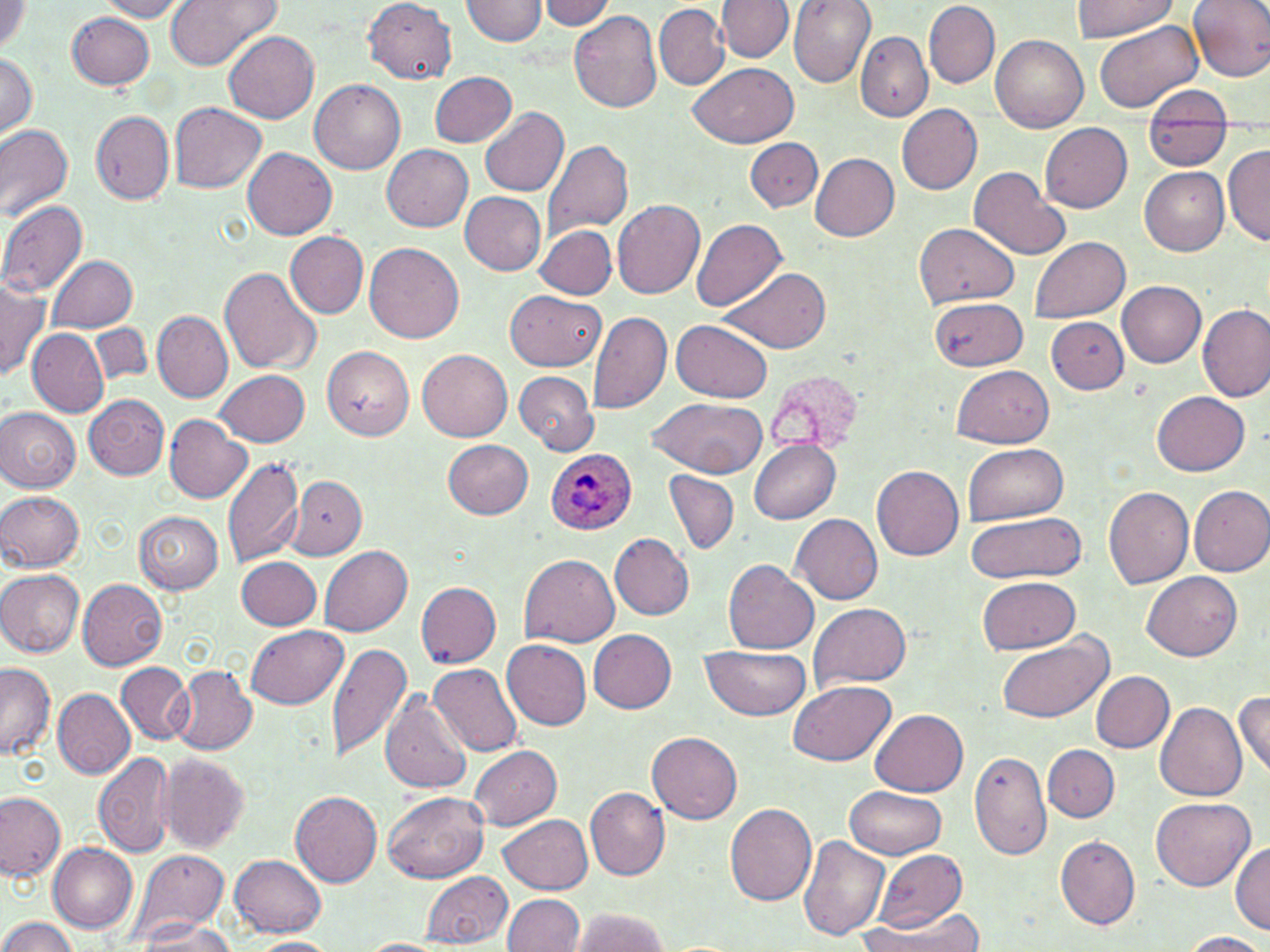
Approximate bounding boxes as (x1,y1)-(x2,y2) corner pairs in pixels. Uninfected red blood cell locations: (99,0)-(187,20), (165,0)-(280,71), (462,0)-(547,44), (538,0)-(617,30), (787,0)-(876,88), (1072,0)-(1180,40), (1186,0)-(1270,82), (362,1)-(457,83), (718,1)-(795,61), (924,1)-(998,88), (0,2)-(28,55), (654,4)-(728,90), (568,10)-(662,114), (67,12)-(156,90), (1092,19)-(1206,114), (224,30)-(319,123), (855,30)-(933,121), (990,35)-(1088,133), (0,52)-(37,139), (689,62)-(795,148), (431,71)-(516,148), (310,79)-(405,174), (1142,84)-(1235,126), (170,103)-(265,193), (898,104)-(983,194), (480,106)-(568,197), (90,110)-(174,204), (1041,122)-(1132,212), (0,124)-(73,221), (1147,128)-(1233,168), (744,138)-(823,211), (542,139)-(633,242), (382,145)-(472,232), (1222,145)-(1270,247), (244,148)-(337,240), (809,151)-(900,240), (968,167)-(1071,262), (1139,167)-(1230,255), (459,191)-(546,275), (0,199)-(88,297), (613,200)-(705,298), (691,217)-(787,312), (913,222)-(1019,308), (536,225)-(617,298), (286,231)-(368,319), (1028,236)-(1130,323), (365,242)-(463,344), (47,255)-(138,330), (720,265)-(832,353), (219,266)-(321,375), (0,280)-(50,379), (1117,281)-(1206,367), (506,290)-(606,372), (930,298)-(1025,371), (1198,303)-(1270,403), (153,310)-(233,403), (587,310)-(673,413), (1045,316)-(1128,392), (672,318)-(774,402), (90,323)-(153,385), (28,328)-(110,418), (322,344)-(414,439), (417,347)-(511,441), (953,366)-(1054,449), (216,369)-(310,446), (515,372)-(597,453), (1153,392)-(1249,476), (83,394)-(169,480), (649,395)-(769,478), (659,398)-(752,556), (0,407)-(81,492), (164,415)-(252,502), (442,439)-(533,518), (750,440)-(842,523), (962,444)-(1069,524), (222,456)-(305,570), (872,465)-(964,561), (665,470)-(739,555), (289,473)-(368,559), (1103,483)-(1195,589), (1189,485)-(1270,577), (1,491)-(85,571), (134,512)-(223,594), (791,513)-(882,605), (964,513)-(1085,584), (610,533)-(693,620), (320,546)-(412,636), (518,553)-(620,647), (236,556)-(322,629), (724,559)-(818,655), (0,568)-(85,657), (1142,571)-(1243,660), (977,576)-(1082,655), (77,579)-(167,671), (415,581)-(502,667), (809,602)-(911,690), (246,625)-(348,709), (590,630)-(677,713), (994,631)-(1112,724), (502,640)-(592,731), (326,641)-(412,762), (699,646)-(813,720), (0,662)-(55,759), (117,662)-(195,745), (428,663)-(523,756), (169,664)-(258,755), (1090,670)-(1173,752), (789,680)-(896,766), (52,688)-(136,780), (1233,690)-(1269,779), (380,691)-(471,794), (1155,702)-(1248,801), (869,709)-(967,796), (647,732)-(743,824), (468,745)-(563,831), (1044,745)-(1120,822), (969,749)-(1052,861), (93,750)-(177,857), (159,754)-(249,853), (845,783)-(947,859), (585,786)-(671,881), (291,789)-(383,886), (382,790)-(490,883), (0,792)-(65,882), (1152,798)-(1255,891), (724,800)-(817,905), (499,812)-(594,894), (737,816)-(873,926), (798,835)-(889,942), (1056,836)-(1141,929), (1231,841)-(1270,934), (48,842)-(138,931), (126,848)-(229,947), (873,848)-(966,932), (230,854)-(327,936), (421,871)-(513,948), (502,894)-(583,951), (858,906)-(985,951), (566,908)-(669,952), (1,917)-(79,952), (135,919)-(240,951), (1179,931)-(1269,952), (244,937)-(342,952), (355,938)-(449,952). Plasmodium ovale-infected red blood cell locations: (545,449)-(637,535). Slide-level diagnosis: Plasmodium ovale. Image is 1270×952 pixels. 1000x magnification. May-Grünwald-Giemsa stain. One field of a larger specimen. Thin blood film. Optical microscopy.